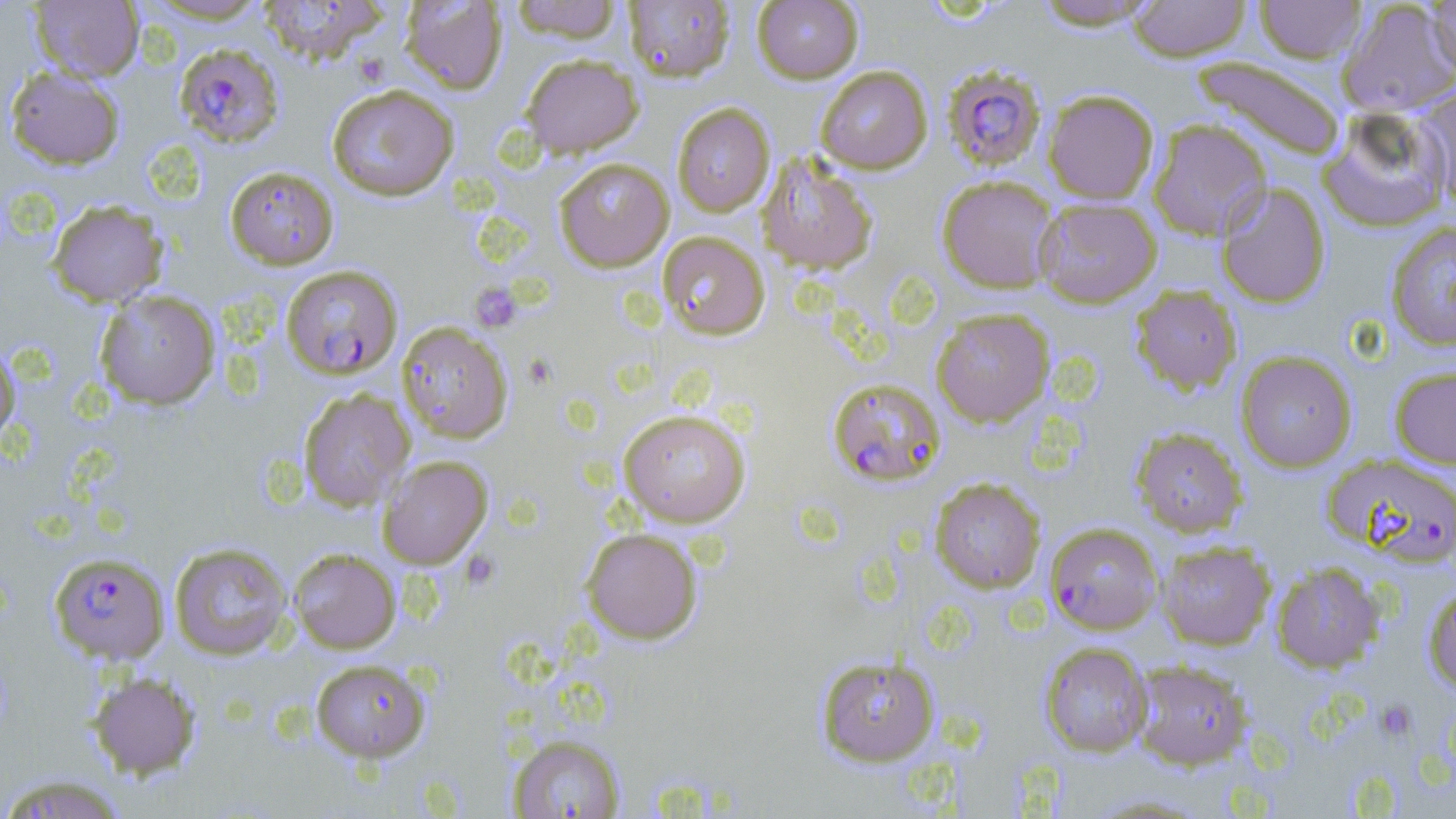 Approximate bounding boxes as named x1/y1/x2/y2 corners in pixels. Plasmodium falciparum-infected red blood cell locations: (x1=174, y1=42, x2=285, y2=148), (x1=941, y1=63, x2=1046, y2=172), (x1=281, y1=265, x2=402, y2=379), (x1=827, y1=377, x2=946, y2=487), (x1=1322, y1=453, x2=1456, y2=566), (x1=1045, y1=522, x2=1163, y2=635), (x1=49, y1=552, x2=169, y2=664). Uninfected red blood cell locations: (x1=30, y1=0, x2=144, y2=82), (x1=139, y1=0, x2=273, y2=24), (x1=257, y1=0, x2=389, y2=65), (x1=400, y1=0, x2=508, y2=93), (x1=510, y1=0, x2=623, y2=42), (x1=623, y1=0, x2=735, y2=82), (x1=752, y1=0, x2=863, y2=83), (x1=1030, y1=0, x2=1161, y2=30), (x1=1127, y1=0, x2=1251, y2=61), (x1=1254, y1=0, x2=1366, y2=63), (x1=1424, y1=0, x2=1456, y2=80), (x1=1338, y1=1, x2=1456, y2=117), (x1=520, y1=54, x2=643, y2=158), (x1=1192, y1=56, x2=1347, y2=162), (x1=5, y1=64, x2=125, y2=170), (x1=815, y1=65, x2=932, y2=173), (x1=326, y1=84, x2=460, y2=201), (x1=1414, y1=84, x2=1456, y2=212), (x1=1043, y1=89, x2=1159, y2=204), (x1=672, y1=103, x2=775, y2=217), (x1=1318, y1=106, x2=1452, y2=233), (x1=1147, y1=118, x2=1272, y2=241), (x1=757, y1=155, x2=878, y2=274), (x1=554, y1=157, x2=674, y2=271), (x1=225, y1=165, x2=339, y2=270), (x1=936, y1=175, x2=1059, y2=293), (x1=1215, y1=182, x2=1331, y2=308), (x1=1033, y1=197, x2=1162, y2=308), (x1=47, y1=199, x2=168, y2=307), (x1=1385, y1=221, x2=1456, y2=350), (x1=657, y1=232, x2=770, y2=340), (x1=1130, y1=285, x2=1242, y2=395), (x1=94, y1=289, x2=220, y2=410), (x1=931, y1=308, x2=1055, y2=427), (x1=397, y1=322, x2=513, y2=443), (x1=0, y1=339, x2=20, y2=447), (x1=1235, y1=350, x2=1357, y2=472), (x1=1389, y1=365, x2=1456, y2=468), (x1=298, y1=388, x2=414, y2=511), (x1=617, y1=408, x2=752, y2=528), (x1=1130, y1=426, x2=1247, y2=537), (x1=377, y1=455, x2=492, y2=569), (x1=930, y1=478, x2=1045, y2=593), (x1=580, y1=527, x2=703, y2=644), (x1=1156, y1=540, x2=1276, y2=650), (x1=169, y1=542, x2=294, y2=660), (x1=288, y1=548, x2=401, y2=653), (x1=1270, y1=561, x2=1386, y2=673), (x1=1423, y1=582, x2=1456, y2=693), (x1=1040, y1=642, x2=1152, y2=757), (x1=815, y1=655, x2=939, y2=766), (x1=310, y1=658, x2=430, y2=761), (x1=1132, y1=661, x2=1253, y2=770), (x1=88, y1=671, x2=201, y2=778), (x1=507, y1=734, x2=625, y2=818), (x1=0, y1=775, x2=129, y2=818). Platelet locations: (x1=470, y1=283, x2=522, y2=332), (x1=1373, y1=699, x2=1417, y2=743). Slide-level diagnosis: Plasmodium falciparum. Thin blood film. Single field of view. May-Grünwald-Giemsa-stained preparation. Light microscopy. Image is 1456×819 pixels. Captured at 1000x magnification.